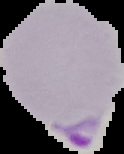
The area outside the segmented cell region is set to black. From a thin blood film. Image is 124×154 pixels. Result: malaria parasites identified.